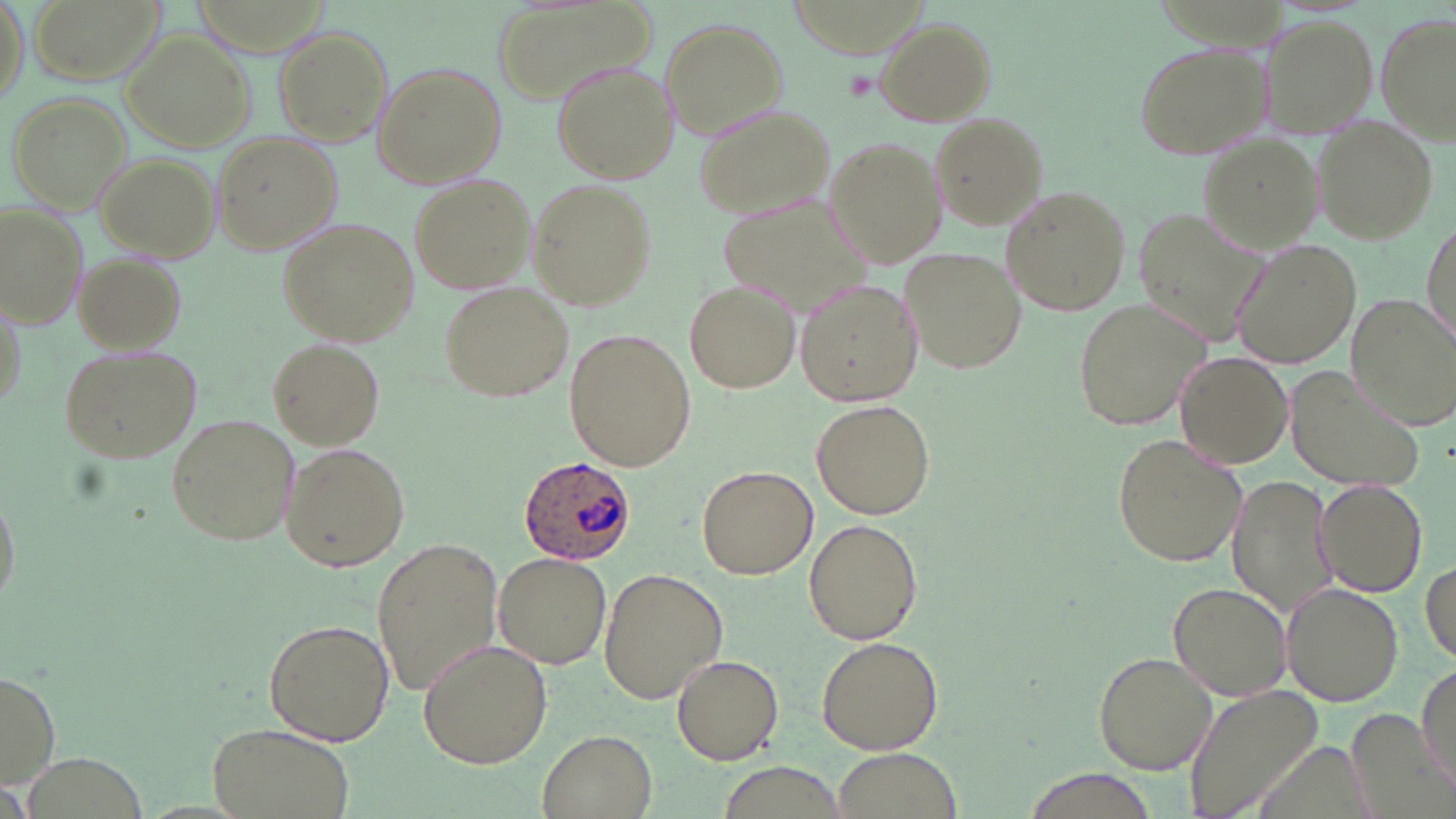
slide_level_diagnosis: Plasmodium ovale
platelet_locations: 'approximate bounding boxes as (x1,y1)-(x2,y2) corner pairs in pixels: (839,69)-(878,103)'
uninfected_red_blood_cell_locations: 'approximate bounding boxes as (x1,y1)-(x2,y2) corner pairs in pixels: (2,0)-(29,108), (27,0)-(164,84), (489,3)-(656,109), (1258,12)-(1381,139), (1381,14)-(1456,141), (658,17)-(788,138), (874,17)-(995,124), (271,25)-(393,147), (121,30)-(257,151), (1132,40)-(1276,159), (372,61)-(508,189), (552,62)-(679,183), (5,92)-(131,209), (691,101)-(839,220), (929,113)-(1047,229), (1312,115)-(1439,245), (824,132)-(948,267), (215,133)-(339,256), (1199,135)-(1326,255), (94,149)-(220,262), (410,174)-(537,295), (530,178)-(657,309), (1000,185)-(1132,320), (715,187)-(878,325), (0,204)-(86,330), (1130,206)-(1273,353), (1422,216)-(1455,343), (277,217)-(419,347), (1234,240)-(1361,371), (900,247)-(1026,375), (75,254)-(185,354), (684,278)-(801,395), (795,278)-(922,407), (439,280)-(574,403), (1073,298)-(1207,430), (1348,298)-(1452,428), (567,328)-(698,471), (268,339)-(384,451), (59,342)-(203,463), (1174,351)-(1293,467), (1288,367)-(1430,492), (811,398)-(936,518), (165,413)-(299,545), (1113,434)-(1245,565), (281,442)-(409,572), (698,465)-(817,579), (1228,472)-(1338,616), (0,480)-(19,613), (1314,480)-(1429,596), (803,517)-(922,646), (373,535)-(503,700), (494,552)-(611,671), (1421,558)-(1455,666), (598,568)-(727,701), (1167,581)-(1291,699), (1282,585)-(1404,706), (265,619)-(395,745), (815,636)-(943,755), (418,639)-(552,769), (1093,651)-(1218,774), (671,652)-(784,765), (1415,662)-(1454,790), (1,669)-(61,788), (1185,684)-(1322,819), (1346,710)-(1456,819), (206,724)-(355,819), (536,729)-(657,818), (833,749)-(959,817), (716,762)-(849,818), (1015,768)-(1159,819)'
plasmodium_ovale_infected_red_blood_cell_locations: 'approximate bounding boxes as (x1,y1)-(x2,y2) corner pairs in pixels: (518,454)-(638,564)'
modality: optical microscopy
stain: May-Grünwald-Giemsa
image_size: 1456×819 pixels
field_of_view: single
preparation: thin blood film
magnification: 1000x